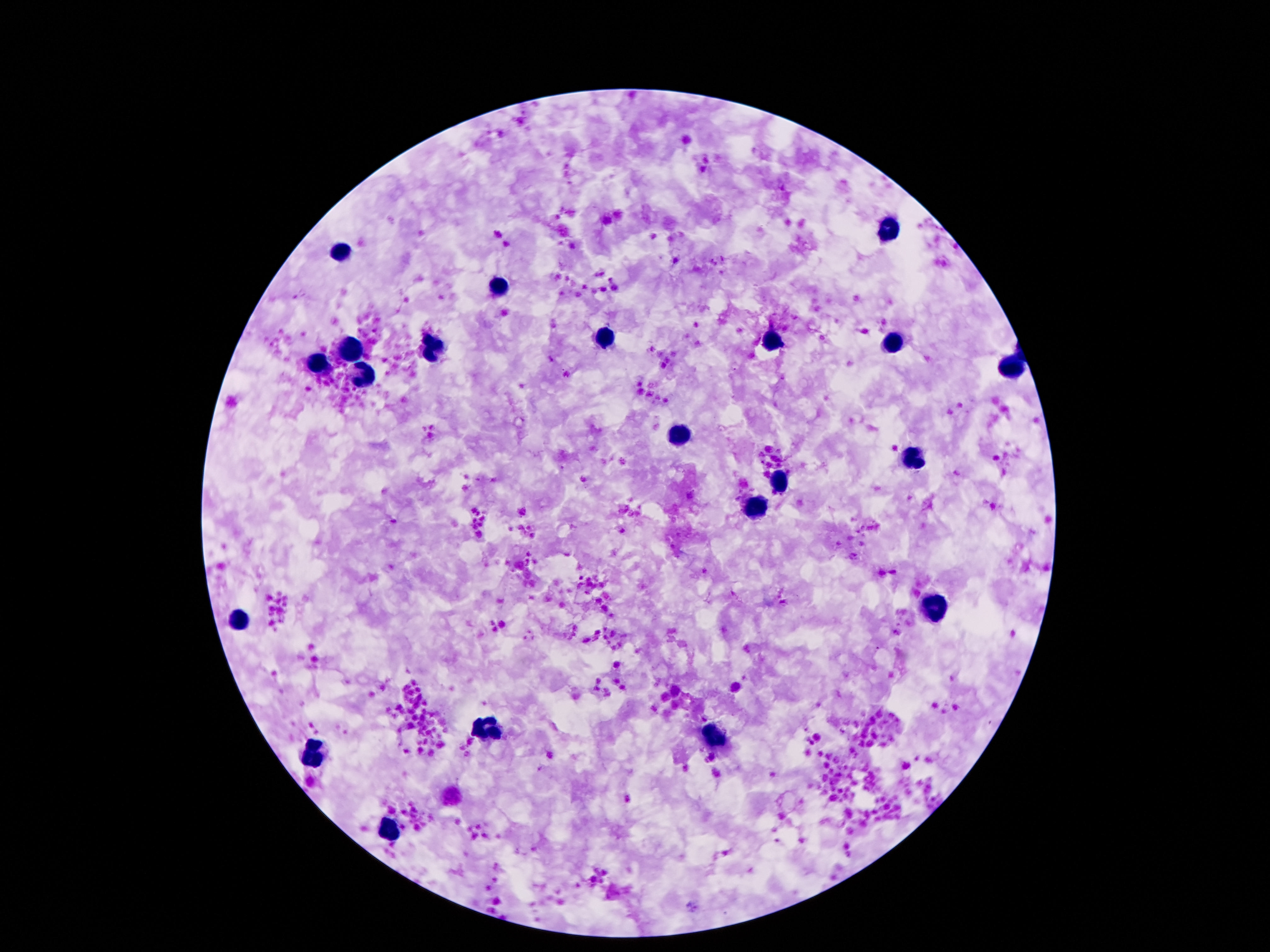
Approximate centers as {x, y} in pixels.
Summary:
  - Leukocyte locations: {893, 229}, {345, 250}, {492, 287}, {607, 339}, {772, 342}, {348, 347}, {430, 347}, {893, 347}, {316, 363}, {1013, 364}, {362, 376}, {676, 435}, {911, 459}, {779, 483}, {760, 508}, {935, 607}, {240, 617}, {484, 728}, {715, 739}, {314, 752}, {389, 827}
  - Stain: Giemsa
  - Patient malaria status: not infected
  - Preparation: thick peripheral-blood smear
  - Image size: 1270×952 pixels
  - Capture: smartphone camera through the microscope eyepiece
  - Field of view: one from this slide
  - Magnification: 100x